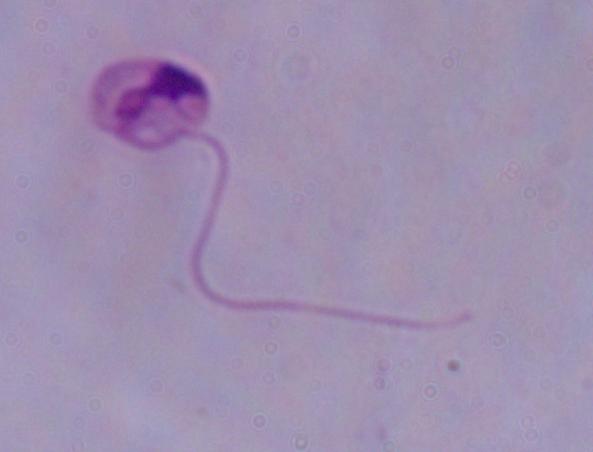
magnification = 1000x
modality = photomicrograph
identification = Leishmania